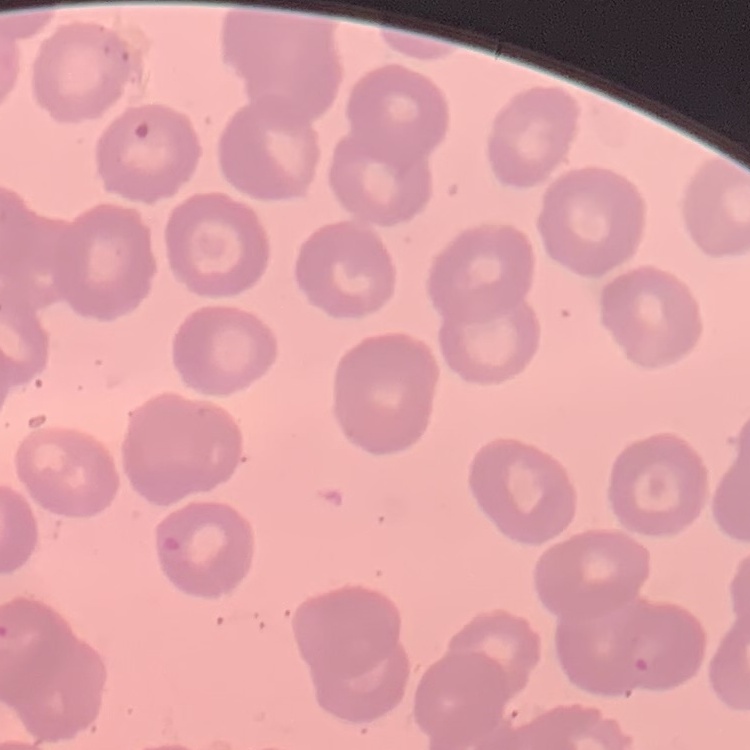

{
  "erythrocyte_morphology": "no rouleaux formation",
  "image_type": "square crop of a larger photomicrograph",
  "stain": "Field's or Giemsa",
  "preparation": "thin blood film"
}